Locate and identify every blood parasite.
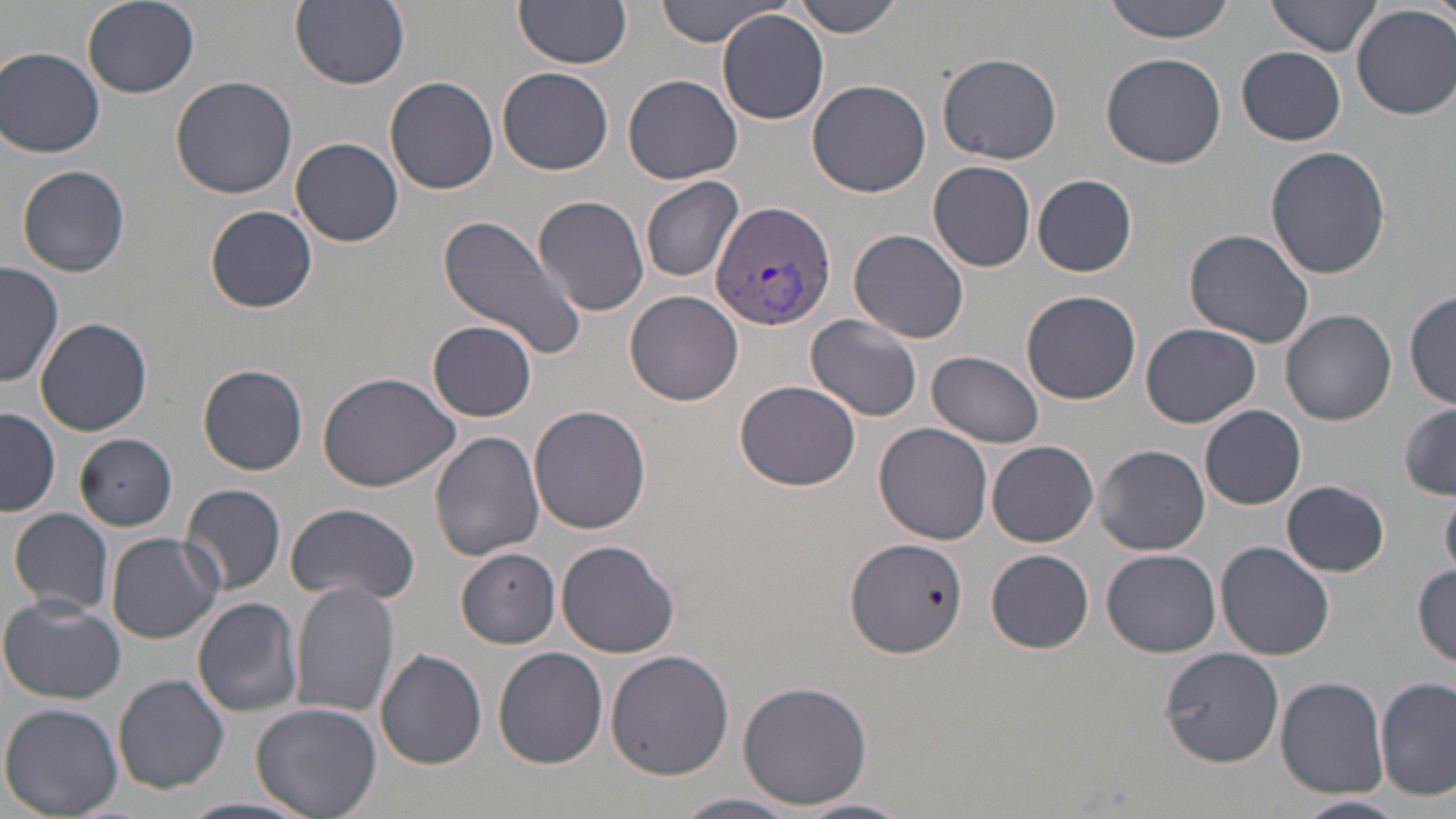

Approximate bounding boxes as [x1, y1, x2, y2] in pixels.
Plasmodium vivax-infected red blood cells: [711, 201, 836, 331].
No Plasmodium falciparum, Plasmodium ovale, Plasmodium malariae, Babesia divergens, or Trypanosoma brucei observed.

Uninfected red blood cell locations: [82, 0, 200, 97], [290, 0, 410, 89], [655, 0, 782, 46], [787, 0, 908, 37], [1103, 0, 1238, 42], [1267, 0, 1383, 57], [517, 2, 632, 68], [1352, 5, 1456, 120], [716, 10, 830, 124], [1238, 46, 1346, 145], [1, 47, 104, 158], [1101, 51, 1227, 169], [938, 52, 1065, 166], [497, 66, 613, 174], [623, 73, 743, 184], [169, 75, 297, 199], [384, 76, 500, 194], [807, 79, 931, 197], [292, 138, 403, 246], [1265, 145, 1391, 281], [929, 160, 1036, 272], [17, 164, 130, 276], [1032, 175, 1138, 277], [640, 178, 745, 282], [532, 194, 653, 313], [204, 204, 318, 313], [438, 213, 588, 362], [1184, 227, 1317, 348], [850, 229, 969, 344], [1, 263, 64, 389], [1021, 289, 1141, 404], [626, 290, 743, 405], [1407, 290, 1455, 409], [1282, 308, 1396, 425], [805, 314, 923, 421], [37, 318, 153, 436], [428, 320, 537, 421], [1141, 323, 1262, 426], [928, 350, 1045, 448], [199, 364, 309, 475], [316, 370, 463, 493], [734, 380, 859, 491], [1200, 404, 1307, 509], [1401, 404, 1456, 498], [529, 405, 651, 534], [1, 407, 59, 516], [875, 422, 993, 544], [429, 430, 544, 560], [74, 434, 177, 530], [988, 440, 1098, 546], [1095, 444, 1209, 554], [1282, 480, 1389, 576], [181, 483, 287, 596], [1442, 487, 1456, 578], [282, 502, 424, 604], [9, 508, 115, 615], [107, 533, 223, 644], [844, 535, 968, 659], [556, 539, 681, 658], [1217, 542, 1335, 661], [458, 548, 562, 648], [988, 549, 1094, 653], [1102, 549, 1221, 657], [1413, 564, 1455, 667], [291, 581, 400, 718], [2, 597, 128, 705], [191, 597, 303, 717], [375, 648, 487, 769], [493, 648, 608, 769], [1162, 648, 1283, 765], [605, 649, 733, 779], [113, 673, 230, 793], [1277, 677, 1389, 798], [1377, 677, 1455, 801], [736, 678, 875, 810], [251, 703, 383, 819], [1, 704, 122, 817], [672, 792, 803, 818], [1293, 794, 1411, 818], [182, 796, 315, 818], [798, 797, 911, 819]. Slide-level diagnosis: Plasmodium vivax. May-Grünwald-Giemsa-stained preparation. Thin blood smear. One field of a larger specimen. Light microscopy. Image is 1456×819 pixels. 1000x magnification.